Report the malaria status of this cell.
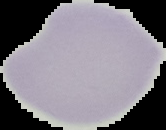

It is uninfected.

Summary:
  - Preparation: thin blood film
  - Image type: segmented cell region on a black background
  - Image size: 166×130 pixels